Describe the morphology of the erythrocytes.
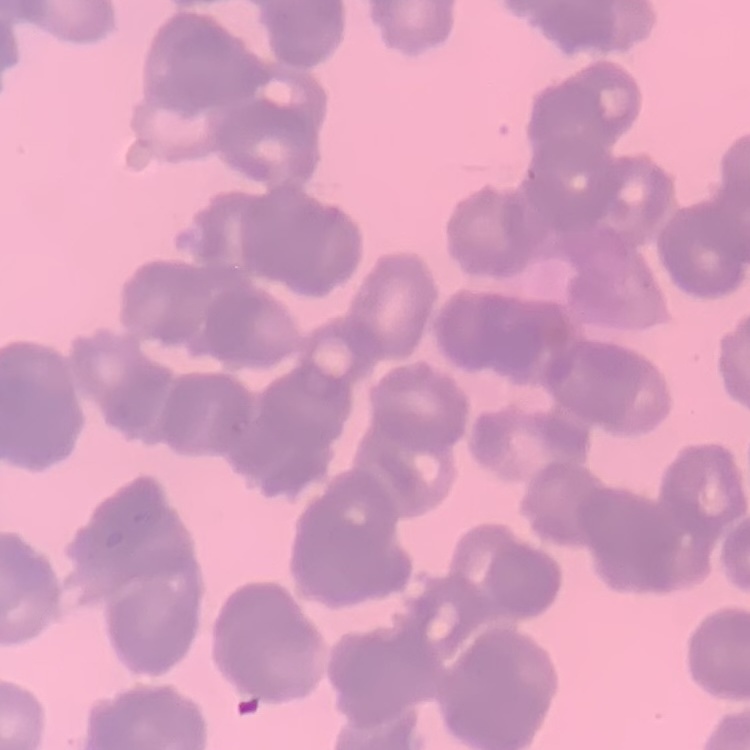
They show rouleaux formation.

stain: Field's or Giemsa
preparation: thin peripheral smear
image_type: one tile cut from a larger photomicrograph